State the blood parasite species.
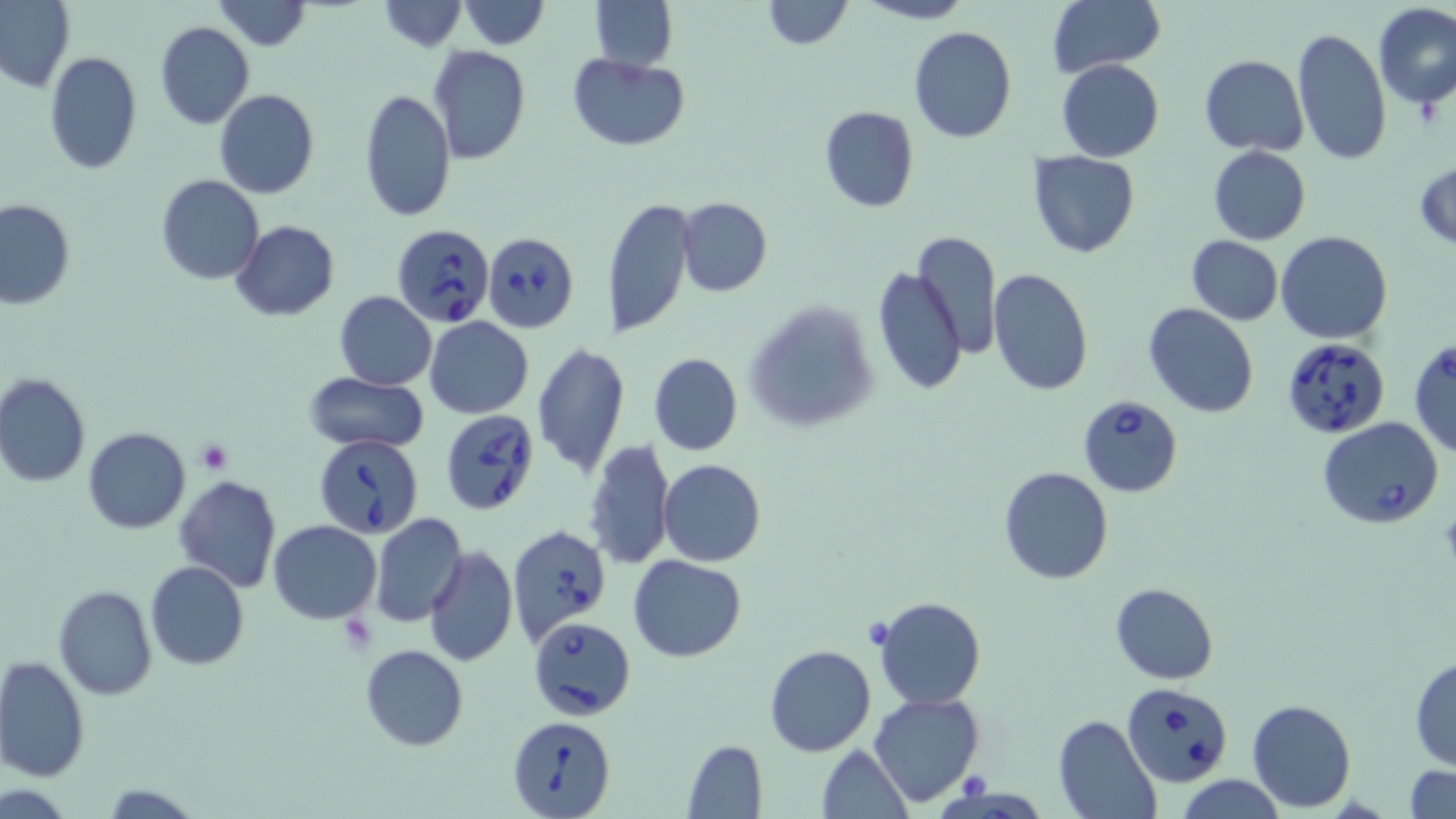
Babesia divergens.

{
  "image_size": "1456×819 pixels",
  "magnification": "1000x",
  "babesia_divergens_infected_red_blood_cell_locations": "approximate bounding boxes as (x1,y1)-(x2,y2) corner pairs in pixels: (392,224)-(495,327), (482,230)-(579,333), (1281,336)-(1391,441), (1409,338)-(1456,457), (1075,392)-(1185,497), (440,410)-(540,517), (1318,417)-(1443,529), (314,435)-(423,537), (507,524)-(612,646), (529,616)-(636,722), (1124,681)-(1233,786), (509,716)-(614,816)",
  "stain": "May-Grünwald-Giemsa",
  "platelet_locations": "approximate bounding boxes as (x1,y1)-(x2,y2) corner pairs in pixels: (195,440)-(233,474), (859,616)-(898,650)",
  "uninfected_red_blood_cell_locations": "approximate bounding boxes as (x1,y1)-(x2,y2) corner pairs in pixels: (0,0)-(75,96), (211,0)-(312,51), (590,0)-(678,72), (760,0)-(852,50), (858,0)-(970,25), (377,1)-(466,51), (460,1)-(549,49), (1046,1)-(1163,78), (1371,1)-(1456,112), (155,21)-(255,130), (908,26)-(1017,143), (1291,27)-(1392,167), (426,46)-(530,164), (44,52)-(142,175), (567,52)-(690,151), (1198,55)-(1309,155), (1056,58)-(1165,162), (214,88)-(320,198), (359,88)-(454,224), (818,106)-(918,213), (1208,146)-(1310,243), (1026,151)-(1143,259), (1414,159)-(1456,251), (157,176)-(265,286), (603,196)-(695,340), (678,198)-(771,297), (0,199)-(75,310), (230,220)-(340,320), (1276,230)-(1394,345), (911,231)-(1001,361), (1186,235)-(1283,325), (872,263)-(967,394), (986,267)-(1096,398), (334,293)-(436,390), (744,298)-(880,432), (1144,303)-(1259,418), (425,316)-(533,419), (531,343)-(630,479), (648,353)-(742,455), (303,371)-(430,451), (0,373)-(90,488), (82,427)-(190,533), (584,438)-(675,572), (658,459)-(767,567), (998,465)-(1113,584), (173,474)-(282,591), (369,511)-(468,628), (267,519)-(382,622), (423,545)-(518,667), (628,555)-(746,661), (146,561)-(249,670), (1110,582)-(1218,683), (54,585)-(157,699), (873,597)-(987,710), (764,644)-(876,756), (359,645)-(468,750), (0,656)-(89,784), (1409,656)-(1456,770), (868,691)-(985,808), (1246,698)-(1356,812), (1052,715)-(1160,819), (683,741)-(767,817), (816,745)-(912,818), (1405,765)-(1456,818), (1176,775)-(1288,819)",
  "modality": "optical microscopy",
  "preparation": "thin blood film",
  "field_of_view": "one of a larger specimen"
}